Name the parasite shown.
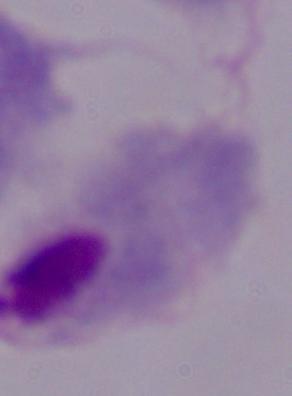
This is a trichomonad.

Summary:
  - Magnification: 1000x
  - Modality: micrograph